State the preparation type.
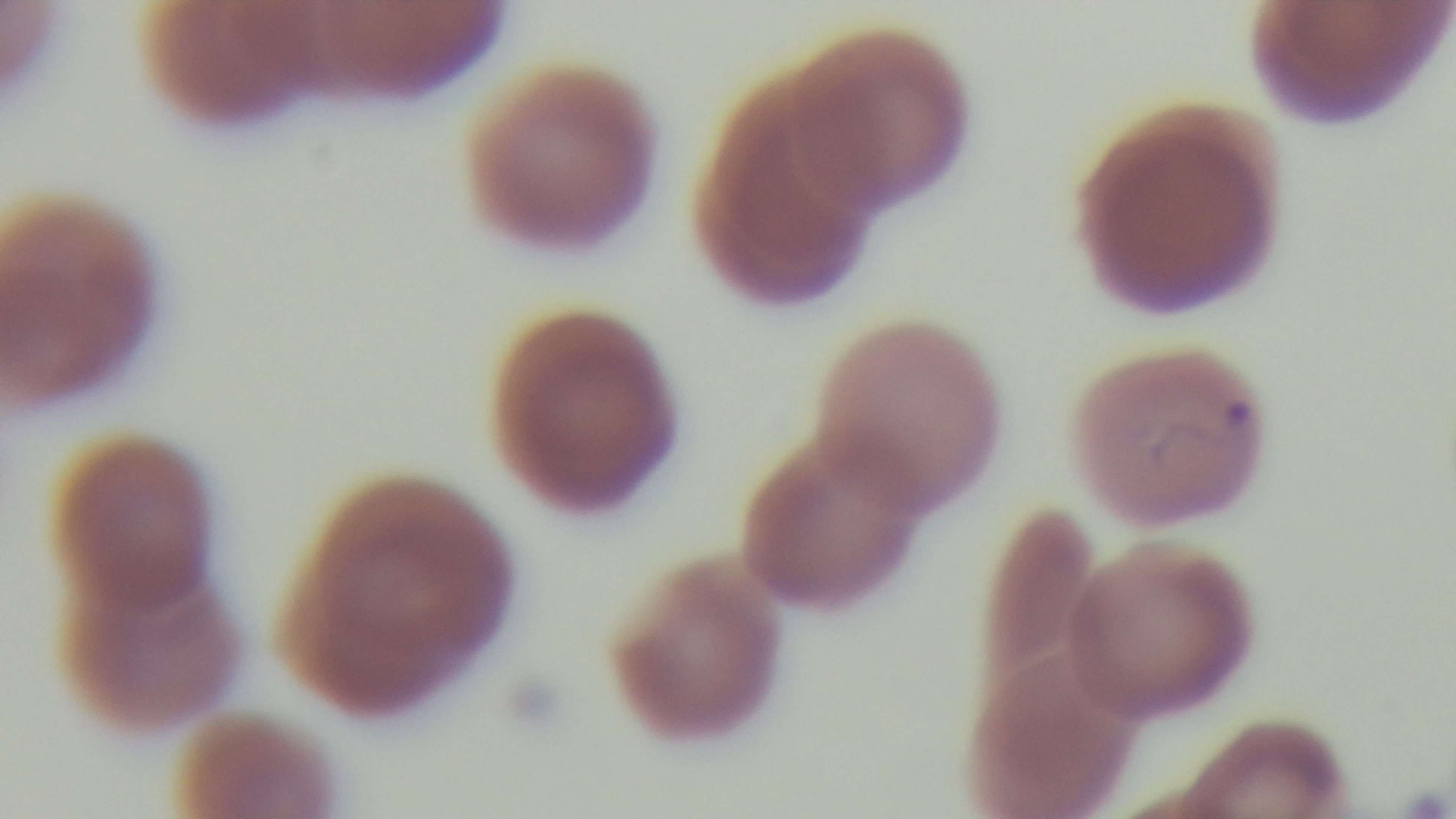

A thin smear.

field of view = one from the slide
malaria status = positive
stain = Giemsa
objective = 100x oil immersion
modality = light microscopy
capture = mounted 4K digital camera